Outline each white blood cell.
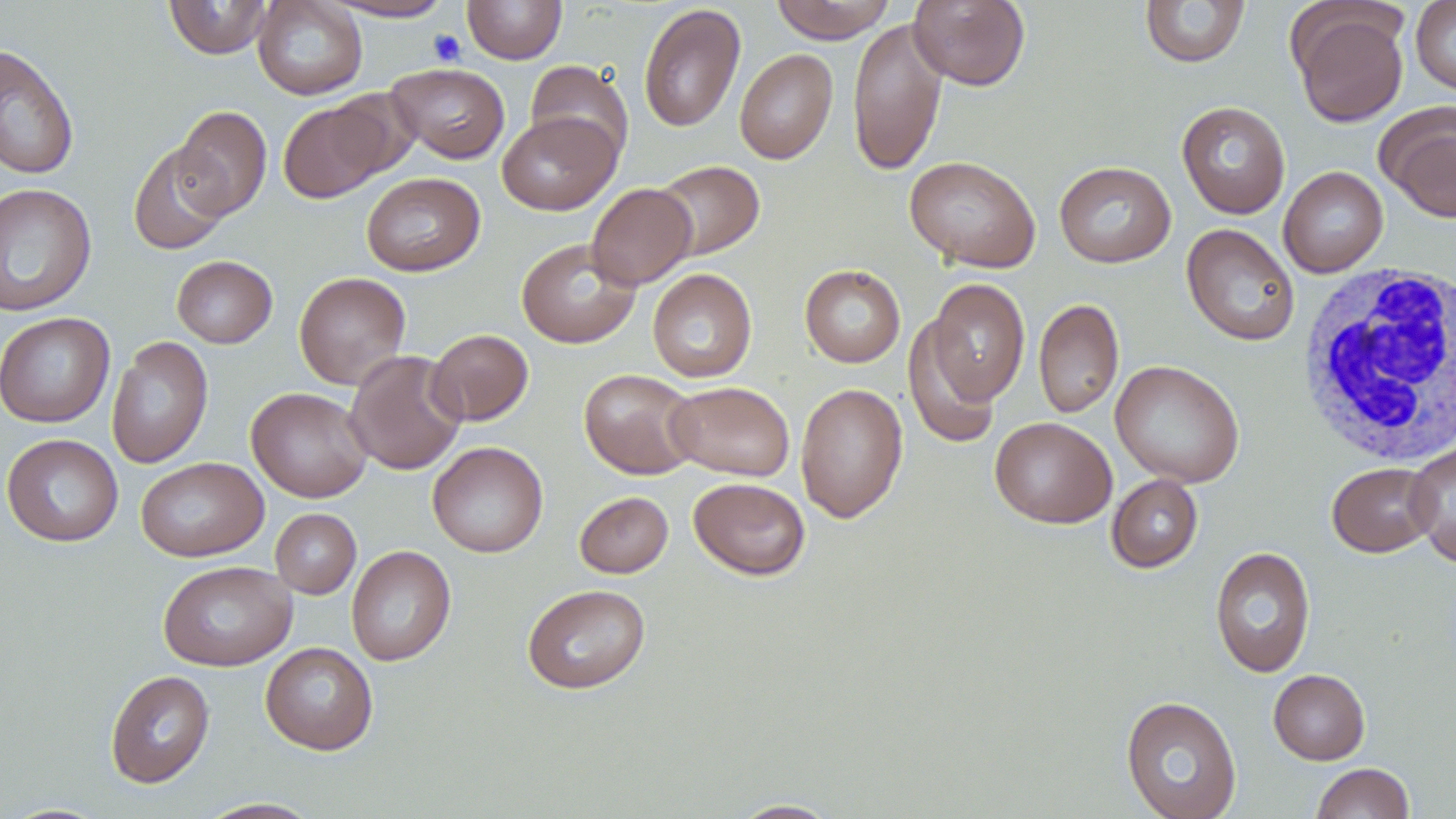

Approximate bounding boxes as (x1, y1, x2, y2) in pixels.
White blood cells: (1296, 261, 1455, 468).

{
  "slide_level_diagnosis": "no evidence of blood parasites",
  "uninfected_red_blood_cell_locations": "approximate bounding boxes as (x1, y1, x2, y2) in pixels: (164, 0, 274, 59), (252, 0, 368, 100), (463, 0, 567, 64), (770, 0, 896, 43), (909, 0, 1030, 90), (1139, 0, 1251, 68), (1410, 0, 1456, 95), (321, 1, 457, 22), (638, 3, 746, 133), (1290, 4, 1409, 127), (847, 16, 948, 177), (0, 43, 79, 180), (734, 48, 838, 164), (525, 60, 634, 165), (386, 63, 510, 164), (278, 99, 392, 202), (1176, 101, 1290, 219), (1377, 102, 1456, 222), (172, 105, 272, 219), (497, 111, 621, 215), (128, 141, 232, 255), (904, 155, 1041, 272), (653, 159, 764, 260), (1054, 161, 1176, 268), (1278, 166, 1388, 277), (361, 172, 485, 276), (0, 182, 96, 316), (586, 183, 697, 290), (1182, 223, 1300, 347), (516, 237, 640, 349), (171, 255, 277, 348), (799, 264, 906, 367), (647, 268, 758, 383), (294, 271, 411, 390), (925, 278, 1030, 408), (1033, 297, 1124, 420), (0, 311, 115, 428), (903, 315, 1002, 450), (426, 328, 533, 426), (106, 336, 213, 469), (345, 349, 467, 475), (1110, 359, 1245, 488), (578, 369, 701, 479), (666, 381, 795, 481), (795, 382, 908, 523), (246, 387, 373, 503), (990, 416, 1117, 529), (1, 433, 124, 547), (427, 441, 548, 559), (1404, 441, 1456, 567), (136, 456, 268, 562), (1326, 462, 1439, 557), (1106, 474, 1203, 573), (688, 477, 811, 580), (574, 491, 673, 578), (270, 508, 361, 598), (346, 545, 456, 667), (1210, 546, 1315, 678), (157, 560, 296, 671), (522, 584, 651, 694), (260, 642, 378, 755), (105, 669, 214, 788), (1268, 669, 1370, 765), (1120, 695, 1242, 819), (1310, 763, 1415, 819), (196, 798, 323, 818), (727, 798, 842, 818)",
  "image_size": "1456×819 pixels",
  "field_of_view": "one of a larger specimen",
  "magnification": "1000x",
  "modality": "light microscopy",
  "stain": "May-Grünwald-Giemsa",
  "platelet_locations": "approximate bounding boxes as (x1, y1, x2, y2) in pixels: (428, 29, 466, 66)",
  "preparation": "thin blood smear"
}